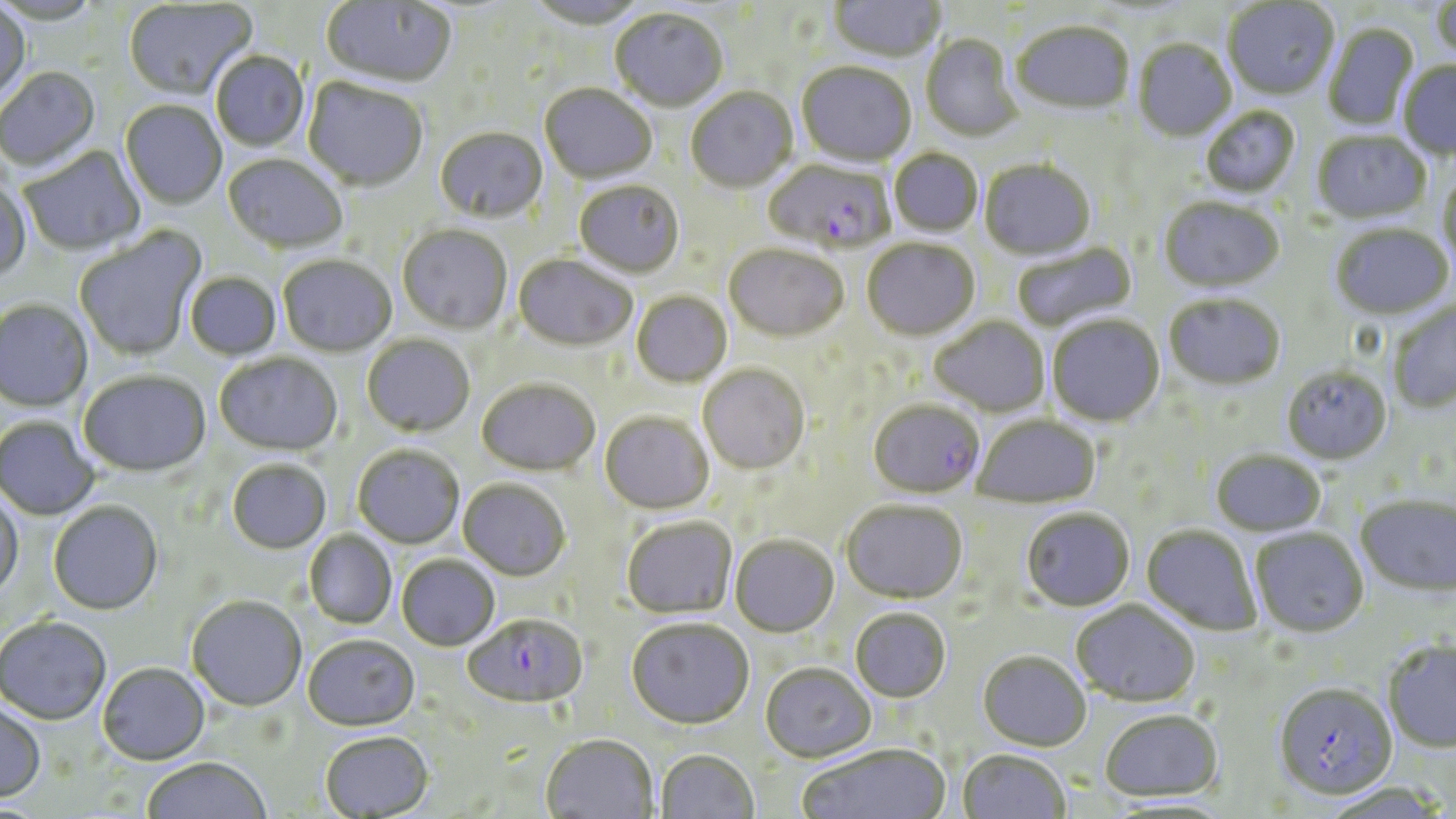
Approximate bounding boxes as named x1/y1/x2/y2 corners in pixels. Plasmodium falciparum-infected red blood cell locations: (x1=764, y1=159, x2=896, y2=255), (x1=868, y1=400, x2=984, y2=499), (x1=463, y1=615, x2=589, y2=711), (x1=1273, y1=683, x2=1397, y2=800). Uninfected red blood cell locations: (x1=828, y1=0, x2=946, y2=64), (x1=1431, y1=0, x2=1456, y2=64), (x1=122, y1=1, x2=256, y2=102), (x1=321, y1=1, x2=457, y2=90), (x1=523, y1=1, x2=649, y2=31), (x1=1223, y1=1, x2=1339, y2=101), (x1=0, y1=4, x2=30, y2=109), (x1=610, y1=9, x2=728, y2=114), (x1=1011, y1=23, x2=1135, y2=117), (x1=1322, y1=24, x2=1420, y2=132), (x1=921, y1=34, x2=1023, y2=143), (x1=1133, y1=40, x2=1236, y2=143), (x1=210, y1=52, x2=310, y2=152), (x1=1398, y1=62, x2=1456, y2=160), (x1=796, y1=63, x2=917, y2=169), (x1=0, y1=67, x2=100, y2=172), (x1=303, y1=79, x2=428, y2=192), (x1=539, y1=84, x2=656, y2=185), (x1=685, y1=88, x2=798, y2=194), (x1=120, y1=101, x2=227, y2=209), (x1=1200, y1=107, x2=1301, y2=199), (x1=435, y1=128, x2=548, y2=224), (x1=1312, y1=131, x2=1430, y2=225), (x1=19, y1=147, x2=145, y2=256), (x1=889, y1=149, x2=983, y2=238), (x1=222, y1=154, x2=348, y2=255), (x1=979, y1=160, x2=1096, y2=261), (x1=1437, y1=169, x2=1456, y2=272), (x1=0, y1=176, x2=31, y2=284), (x1=574, y1=181, x2=685, y2=279), (x1=1158, y1=199, x2=1285, y2=294), (x1=1330, y1=224, x2=1454, y2=321), (x1=397, y1=225, x2=512, y2=336), (x1=73, y1=227, x2=207, y2=362), (x1=862, y1=238, x2=980, y2=342), (x1=1011, y1=241, x2=1137, y2=333), (x1=724, y1=245, x2=849, y2=343), (x1=277, y1=255, x2=397, y2=358), (x1=514, y1=255, x2=637, y2=352), (x1=185, y1=272, x2=281, y2=360), (x1=631, y1=291, x2=732, y2=388), (x1=1164, y1=294, x2=1286, y2=392), (x1=1387, y1=299, x2=1456, y2=414), (x1=0, y1=300, x2=92, y2=412), (x1=1046, y1=315, x2=1165, y2=427), (x1=930, y1=316, x2=1050, y2=418), (x1=362, y1=334, x2=475, y2=437), (x1=214, y1=353, x2=343, y2=456), (x1=698, y1=364, x2=810, y2=475), (x1=1281, y1=366, x2=1393, y2=465), (x1=78, y1=370, x2=210, y2=478), (x1=477, y1=378, x2=600, y2=476), (x1=600, y1=412, x2=714, y2=515), (x1=973, y1=414, x2=1100, y2=508), (x1=0, y1=416, x2=100, y2=521), (x1=352, y1=445, x2=465, y2=549), (x1=1210, y1=450, x2=1326, y2=537), (x1=227, y1=459, x2=332, y2=554), (x1=458, y1=479, x2=570, y2=581), (x1=0, y1=493, x2=24, y2=598), (x1=1355, y1=494, x2=1455, y2=598), (x1=48, y1=502, x2=164, y2=615), (x1=841, y1=502, x2=967, y2=604), (x1=1021, y1=508, x2=1135, y2=613), (x1=622, y1=516, x2=737, y2=620), (x1=1141, y1=525, x2=1262, y2=636), (x1=1250, y1=527, x2=1368, y2=637), (x1=304, y1=530, x2=397, y2=629), (x1=730, y1=536, x2=839, y2=638), (x1=396, y1=555, x2=500, y2=652), (x1=186, y1=595, x2=307, y2=712), (x1=1071, y1=600, x2=1200, y2=708), (x1=850, y1=608, x2=952, y2=703), (x1=0, y1=615, x2=111, y2=725), (x1=626, y1=619, x2=754, y2=731), (x1=302, y1=635, x2=420, y2=733), (x1=1382, y1=639, x2=1456, y2=752), (x1=978, y1=652, x2=1091, y2=752), (x1=97, y1=662, x2=210, y2=765), (x1=760, y1=664, x2=876, y2=764), (x1=0, y1=702, x2=46, y2=803), (x1=1099, y1=710, x2=1224, y2=803), (x1=321, y1=732, x2=434, y2=818), (x1=540, y1=735, x2=659, y2=819), (x1=797, y1=745, x2=950, y2=819), (x1=957, y1=750, x2=1071, y2=819), (x1=656, y1=751, x2=759, y2=819), (x1=140, y1=757, x2=272, y2=818). Slide-level diagnosis: Plasmodium falciparum. One field of a larger specimen. Optical microscopy. May-Grünwald-Giemsa-stained preparation. Captured at 1000x magnification. Thin blood film. Image is 1456×819 pixels.